Assess the morphology of the erythrocytes.
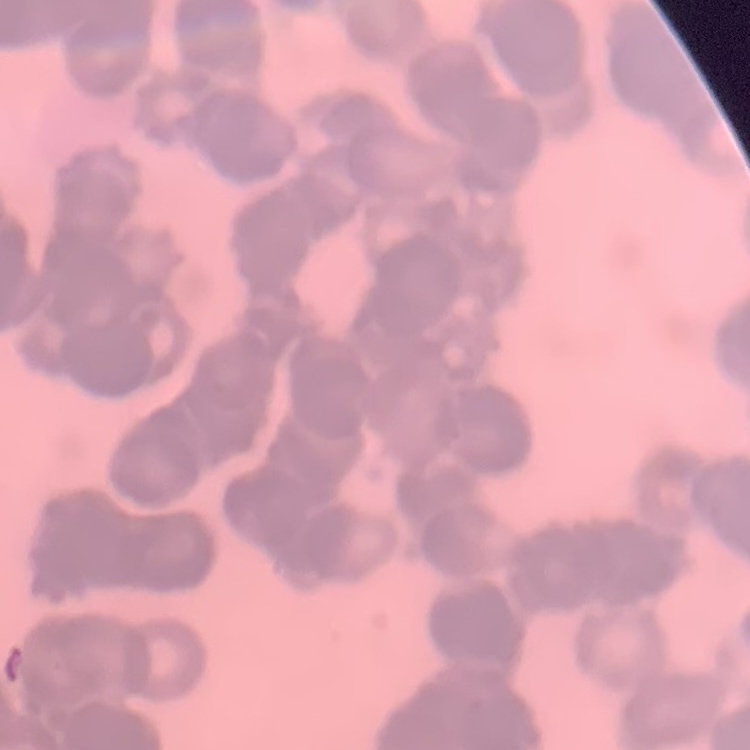
Rouleaux formation.

Summary:
  - Preparation: thin peripheral smear
  - Image type: one tile cut from a larger photomicrograph
  - Stain: Field's or Giemsa